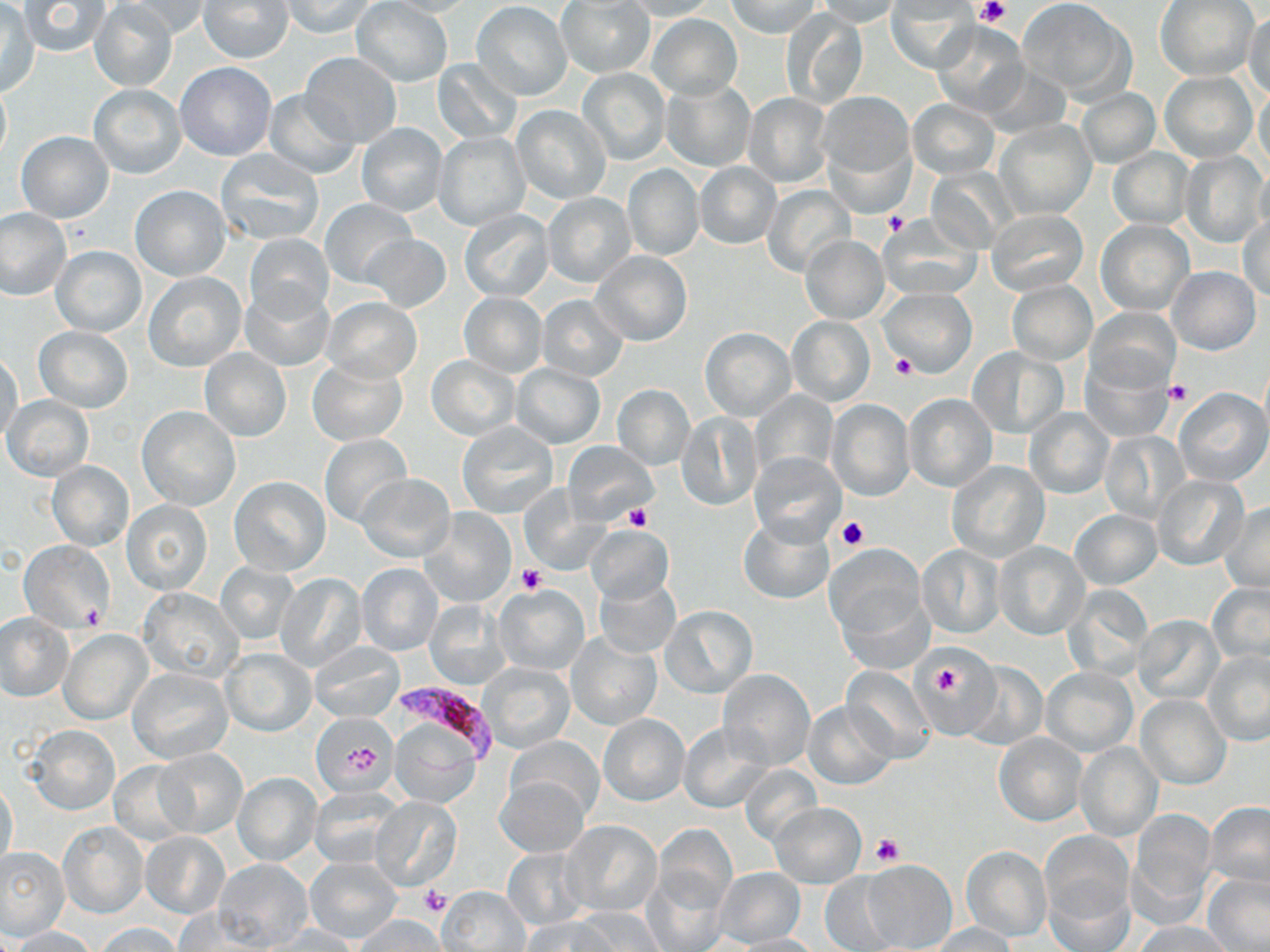

{
  "slide_level_diagnosis": "Plasmodium falciparum",
  "magnification": "1000x",
  "field_of_view": "single",
  "uninfected_red_blood_cell_locations": "approximate bounding boxes as [x1, y1, x2, y2] in pixels: [89, 0, 177, 91], [120, 0, 212, 39], [198, 0, 294, 63], [281, 0, 377, 38], [378, 0, 480, 17], [555, 0, 656, 79], [623, 0, 717, 20], [727, 0, 822, 39], [1017, 0, 1137, 103], [19, 1, 110, 57], [351, 1, 453, 87], [814, 1, 905, 27], [1155, 1, 1259, 82], [471, 2, 572, 100], [885, 3, 976, 72], [0, 4, 39, 95], [779, 8, 869, 110], [1243, 11, 1269, 99], [647, 13, 742, 100], [931, 23, 1029, 117], [300, 52, 402, 147], [433, 58, 523, 146], [175, 61, 277, 161], [577, 67, 671, 165], [1160, 71, 1258, 162], [0, 79, 11, 167], [660, 79, 755, 171], [1254, 82, 1269, 174], [88, 84, 186, 178], [262, 88, 358, 179], [1075, 88, 1161, 168], [817, 90, 915, 186], [743, 92, 832, 187], [908, 99, 999, 180], [512, 106, 611, 204], [994, 118, 1095, 220], [356, 123, 447, 217], [16, 131, 114, 222], [433, 132, 531, 231], [215, 148, 324, 245], [1108, 148, 1194, 230], [1181, 151, 1270, 249], [694, 162, 781, 249], [622, 164, 704, 261], [925, 165, 1018, 252], [132, 185, 230, 280], [763, 185, 855, 279], [544, 193, 635, 287], [321, 198, 416, 287], [0, 208, 71, 301], [459, 210, 554, 302], [986, 210, 1089, 295], [1238, 212, 1270, 303], [878, 215, 982, 299], [1096, 220, 1194, 315], [244, 233, 333, 318], [361, 233, 450, 313], [801, 235, 889, 324], [51, 245, 146, 337], [591, 251, 692, 345], [1168, 267, 1260, 355], [143, 271, 246, 372], [1007, 280, 1096, 364], [239, 283, 334, 372], [878, 287, 977, 377], [459, 293, 547, 377], [538, 295, 628, 381], [323, 297, 422, 382], [1085, 307, 1180, 394], [786, 316, 874, 406], [34, 326, 133, 412], [700, 327, 796, 421], [968, 346, 1068, 439], [200, 348, 291, 442], [1, 351, 22, 442], [427, 355, 519, 440], [307, 357, 407, 445], [1082, 358, 1173, 442], [511, 363, 605, 448], [613, 384, 695, 470], [1174, 388, 1269, 486], [751, 391, 836, 478], [903, 393, 997, 492], [3, 395, 94, 482], [825, 400, 916, 501], [137, 407, 241, 510], [1025, 409, 1112, 498], [677, 413, 761, 511], [456, 421, 560, 519], [1100, 432, 1191, 524], [320, 435, 414, 530], [562, 441, 657, 527], [751, 451, 846, 545], [47, 460, 135, 551], [947, 461, 1049, 562], [36, 463, 123, 630], [357, 474, 455, 561], [1152, 474, 1250, 571], [229, 477, 330, 577], [517, 487, 605, 573], [121, 499, 212, 595], [1221, 501, 1270, 592], [420, 508, 517, 609], [1071, 510, 1161, 590], [737, 516, 835, 604], [587, 525, 670, 602], [19, 540, 113, 630], [994, 541, 1090, 641], [825, 544, 928, 650], [917, 544, 1004, 639], [356, 561, 443, 656], [216, 562, 298, 644], [275, 574, 366, 672], [594, 576, 680, 659], [1208, 581, 1270, 671], [1062, 583, 1152, 681], [494, 584, 589, 676], [138, 590, 246, 684], [424, 599, 512, 689], [661, 606, 757, 698], [1, 614, 73, 700], [1132, 614, 1225, 706], [58, 629, 151, 725], [565, 632, 661, 732], [309, 642, 404, 723], [221, 647, 316, 737], [917, 650, 995, 727], [1204, 651, 1270, 747], [480, 661, 575, 753], [961, 662, 1048, 749], [1040, 666, 1137, 755], [842, 667, 937, 763], [129, 668, 234, 763], [718, 669, 815, 769], [1136, 694, 1230, 789], [803, 701, 897, 789], [311, 712, 397, 796], [598, 715, 689, 806], [389, 717, 482, 807], [678, 722, 774, 813], [27, 724, 121, 815], [994, 734, 1088, 826], [506, 736, 602, 819], [1075, 741, 1163, 840], [154, 750, 247, 837], [108, 761, 195, 845], [738, 765, 822, 847], [233, 772, 321, 865], [496, 777, 588, 856], [1, 781, 18, 870], [309, 786, 404, 869], [371, 797, 462, 889], [770, 802, 867, 888], [1204, 802, 1270, 891], [1127, 810, 1218, 922], [562, 820, 662, 917], [58, 821, 148, 918], [651, 825, 736, 914], [1039, 830, 1133, 927], [140, 832, 231, 918], [0, 846, 70, 940], [961, 846, 1051, 942], [503, 848, 589, 929], [304, 857, 404, 944], [213, 859, 313, 950], [862, 859, 957, 952], [643, 867, 729, 951], [713, 867, 805, 946], [820, 870, 901, 951], [1043, 874, 1135, 952], [1202, 874, 1269, 950], [439, 887, 532, 951], [567, 907, 666, 952], [173, 908, 273, 952], [358, 914, 444, 950], [524, 918, 613, 951], [1134, 921, 1230, 952], [95, 923, 184, 952], [929, 923, 1017, 952], [267, 924, 359, 951], [10, 926, 97, 952], [727, 933, 820, 952]",
  "platelet_locations": "approximate bounding boxes as [x1, y1, x2, y2] in pixels: [976, 0, 1010, 26], [883, 212, 909, 236], [890, 354, 918, 380], [1164, 378, 1192, 406], [623, 505, 652, 532], [837, 516, 869, 551], [519, 565, 547, 594], [79, 602, 107, 629], [925, 655, 972, 707], [870, 834, 905, 868], [420, 885, 449, 916]",
  "preparation": "thin blood film",
  "image_size": "1270×952 pixels",
  "stain": "May-Grünwald-Giemsa",
  "modality": "light microscopy",
  "plasmodium_falciparum_infected_red_blood_cell_locations": "approximate bounding boxes as [x1, y1, x2, y2] in pixels: [398, 677, 506, 776]"
}